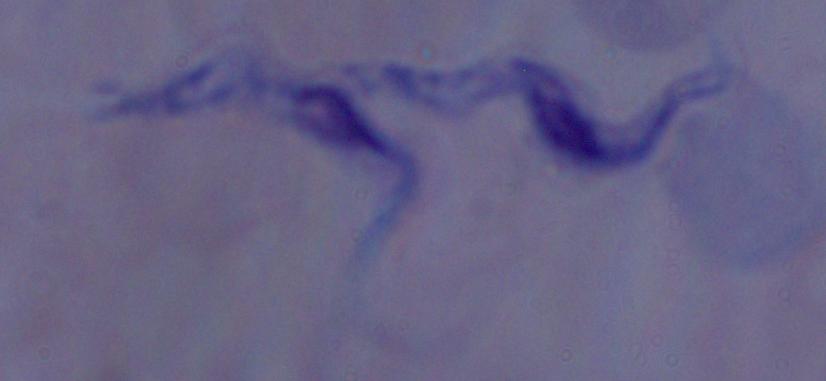

modality = micrograph
identification = trypanosome
magnification = 1000x